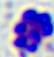

Summary:
  - Identification: white blood cell
  - Modality: photomicrograph
  - Magnification: 400x